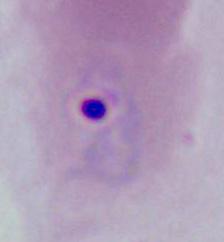

A Plasmodium parasite is shown. Captured at either 400x or 1000x magnification. Photomicrograph.